Assess this cell for malaria.
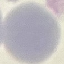

It is uninfected.

Photographed with a smartphone camera at the microscope eyepiece. Giemsa stain. Thin blood smear. Automatically extracted cell patch, resized to 64 × 64 pixels.